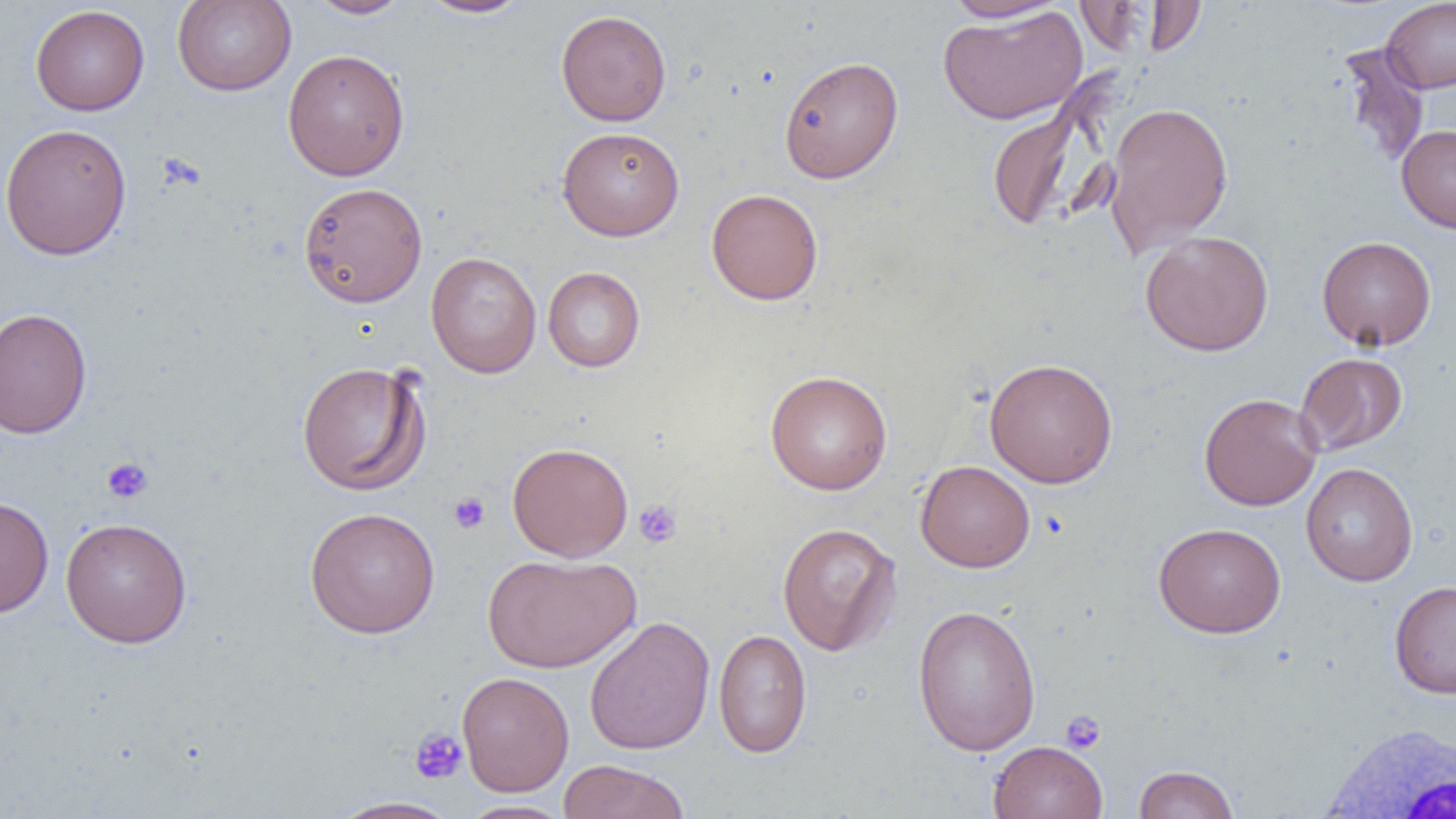
slide_level_diagnosis: negative for blood parasites
white_blood_cell_locations: 'approximate bounding boxes as (x1, y1, x2, y2) in pixels: (1314, 722, 1455, 817)'
modality: optical microscopy
magnification: 1000x
platelet_locations: 'approximate bounding boxes as (x1, y1, x2, y2) in pixels: (101, 457, 153, 504), (448, 492, 490, 533), (633, 499, 682, 548), (1060, 710, 1106, 754), (409, 727, 468, 784)'
uninfected_red_blood_cell_locations: 'approximate bounding boxes as (x1, y1, x2, y2) in pixels: (172, 0, 296, 96), (306, 0, 411, 18), (417, 0, 533, 18), (943, 0, 1070, 23), (1144, 0, 1207, 57), (1381, 0, 1456, 93), (30, 5, 149, 116), (937, 6, 1088, 124), (556, 9, 672, 126), (1336, 41, 1431, 169), (282, 48, 410, 181), (778, 56, 904, 183), (987, 100, 1095, 233), (1103, 101, 1234, 253), (0, 123, 132, 261), (1396, 124, 1456, 234), (557, 126, 685, 241), (299, 182, 427, 307), (705, 188, 824, 305), (1140, 230, 1274, 356), (1316, 236, 1437, 351), (426, 251, 542, 378), (543, 266, 645, 372), (0, 307, 92, 438), (1295, 352, 1408, 456), (984, 357, 1118, 488), (296, 360, 430, 496), (765, 369, 892, 495), (1199, 393, 1322, 510), (506, 442, 634, 561), (915, 460, 1035, 572), (1300, 462, 1418, 586), (0, 496, 54, 619), (304, 506, 440, 638), (60, 516, 193, 648), (1154, 521, 1286, 638), (777, 522, 902, 656), (483, 552, 642, 672), (1388, 580, 1456, 698), (912, 604, 1041, 755), (584, 616, 715, 755), (713, 628, 812, 757), (457, 671, 574, 796), (988, 740, 1108, 819), (557, 759, 690, 819), (1133, 764, 1239, 819), (328, 796, 462, 818), (456, 800, 574, 819)'
field_of_view: single
preparation: thin blood smear
image_size: 1456×819 pixels